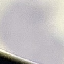

malaria status = uninfected
preparation = thin smear
image type = automatically extracted cell patch, resized to 64 × 64 pixels
stain = Giemsa
capture = smartphone camera at the microscope eyepiece